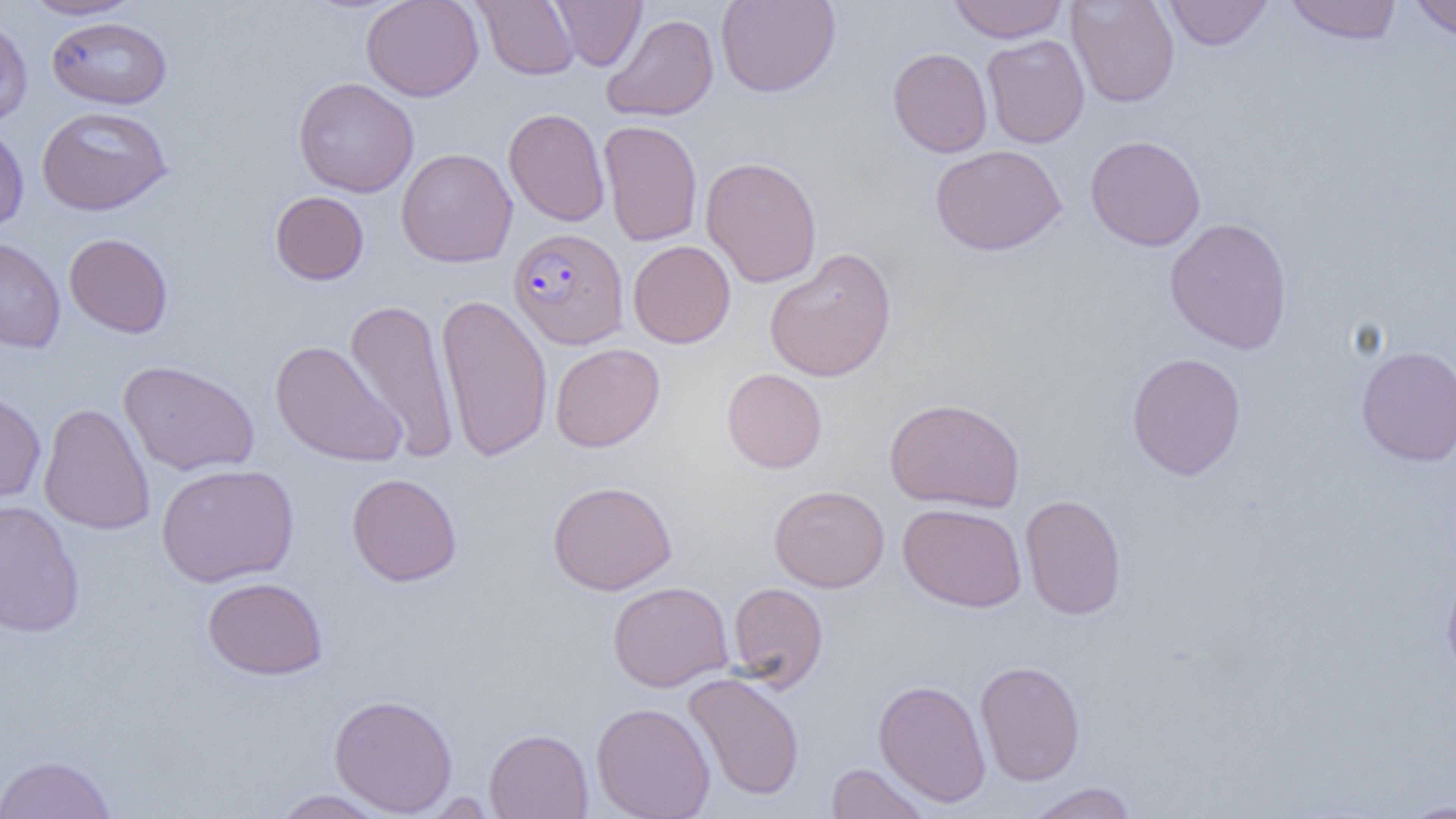

Summary:
  - Coordinate format: approximate bounding boxes as [x1, y1, x2, y2] in pixels
  - Uninfected red blood cell locations: [19, 0, 142, 20], [360, 0, 484, 102], [473, 0, 580, 80], [549, 0, 646, 70], [716, 0, 841, 97], [948, 0, 1068, 43], [1067, 0, 1180, 108], [1163, 0, 1273, 50], [1408, 0, 1456, 41], [1284, 1, 1403, 45], [601, 13, 719, 122], [0, 15, 33, 128], [46, 17, 173, 108], [981, 34, 1090, 148], [887, 47, 992, 158], [294, 77, 419, 197], [36, 106, 172, 216], [503, 107, 611, 226], [598, 120, 702, 246], [0, 121, 29, 233], [1085, 134, 1206, 251], [930, 144, 1066, 255], [396, 148, 518, 268], [700, 156, 822, 288], [269, 191, 370, 286], [1164, 217, 1293, 355], [63, 233, 174, 338], [0, 236, 66, 353], [628, 240, 736, 348], [764, 247, 896, 382], [436, 293, 554, 463], [343, 297, 460, 462], [270, 340, 408, 468], [550, 343, 665, 452], [1356, 345, 1456, 466], [1126, 352, 1247, 480], [118, 359, 260, 476], [722, 368, 827, 473], [0, 389, 47, 508], [884, 397, 1026, 513], [38, 403, 155, 535], [156, 463, 299, 587], [346, 473, 462, 586], [548, 480, 677, 595], [769, 484, 889, 592], [1020, 494, 1127, 620], [0, 500, 85, 638], [898, 503, 1027, 612], [1441, 574, 1456, 684], [202, 576, 327, 680], [607, 581, 733, 692], [727, 582, 829, 692], [975, 660, 1086, 785], [683, 672, 805, 801], [873, 679, 991, 807], [329, 693, 458, 816], [591, 702, 716, 819], [484, 728, 593, 819], [0, 754, 118, 818], [825, 762, 931, 818], [1024, 782, 1138, 819], [270, 789, 392, 818], [1395, 798, 1456, 818]
  - Plasmodium falciparum-infected red blood cell locations: [508, 228, 628, 349]
  - Slide-level diagnosis: Plasmodium falciparum
  - Magnification: 1000x
  - Field of view: one of a larger specimen
  - Preparation: thin blood film
  - Image size: 1456×819 pixels
  - Modality: optical microscopy